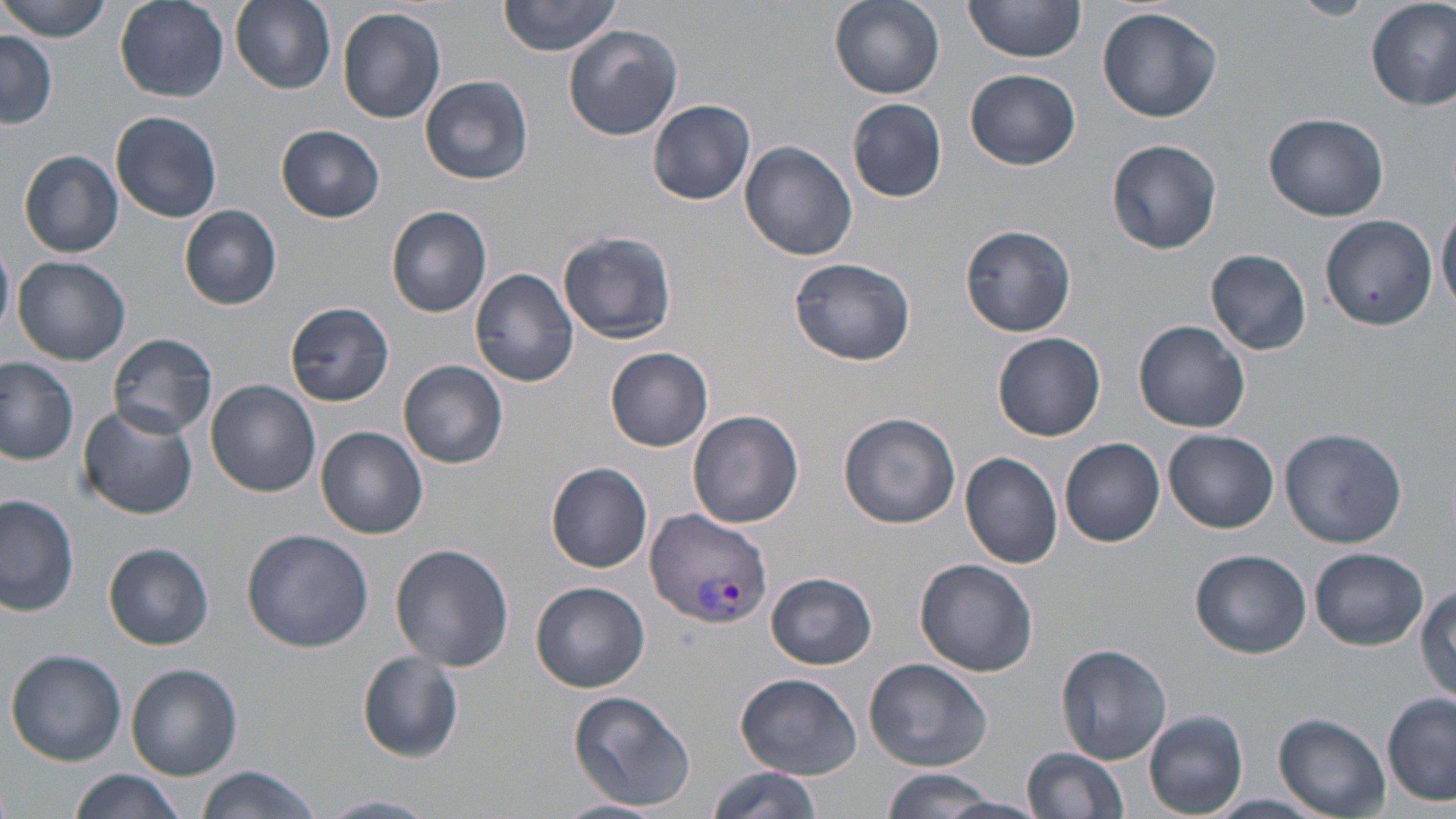 Approximate bounding boxes as named x1/y1/x2/y2 corners in pixels. Uninfected red blood cell locations: (x1=1, y1=0, x2=114, y2=41), (x1=115, y1=0, x2=230, y2=102), (x1=230, y1=0, x2=336, y2=92), (x1=497, y1=0, x2=622, y2=57), (x1=829, y1=0, x2=945, y2=99), (x1=1288, y1=0, x2=1378, y2=21), (x1=1366, y1=0, x2=1456, y2=110), (x1=963, y1=1, x2=1089, y2=67), (x1=1096, y1=5, x2=1224, y2=123), (x1=337, y1=6, x2=447, y2=124), (x1=563, y1=26, x2=683, y2=141), (x1=0, y1=29, x2=57, y2=127), (x1=966, y1=69, x2=1082, y2=168), (x1=420, y1=76, x2=533, y2=185), (x1=847, y1=98, x2=948, y2=203), (x1=648, y1=99, x2=756, y2=203), (x1=110, y1=110, x2=224, y2=222), (x1=1263, y1=111, x2=1387, y2=221), (x1=275, y1=125, x2=386, y2=222), (x1=1106, y1=139, x2=1223, y2=255), (x1=740, y1=142, x2=857, y2=260), (x1=19, y1=150, x2=124, y2=257), (x1=1437, y1=199, x2=1456, y2=314), (x1=179, y1=204, x2=282, y2=309), (x1=386, y1=207, x2=492, y2=317), (x1=1319, y1=215, x2=1436, y2=331), (x1=960, y1=223, x2=1077, y2=337), (x1=559, y1=228, x2=677, y2=346), (x1=0, y1=242, x2=14, y2=339), (x1=1206, y1=248, x2=1312, y2=356), (x1=788, y1=254, x2=914, y2=366), (x1=13, y1=256, x2=130, y2=366), (x1=469, y1=268, x2=580, y2=389), (x1=285, y1=302, x2=395, y2=406), (x1=1135, y1=319, x2=1251, y2=432), (x1=109, y1=331, x2=218, y2=439), (x1=994, y1=331, x2=1106, y2=440), (x1=606, y1=347, x2=714, y2=451), (x1=0, y1=358, x2=78, y2=465), (x1=399, y1=361, x2=508, y2=468), (x1=205, y1=378, x2=320, y2=496), (x1=78, y1=404, x2=198, y2=519), (x1=689, y1=410, x2=805, y2=528), (x1=839, y1=412, x2=960, y2=528), (x1=317, y1=426, x2=427, y2=540), (x1=1279, y1=426, x2=1407, y2=547), (x1=1164, y1=431, x2=1278, y2=533), (x1=1060, y1=438, x2=1166, y2=547), (x1=959, y1=450, x2=1064, y2=568), (x1=546, y1=463, x2=653, y2=573), (x1=0, y1=495, x2=79, y2=615), (x1=240, y1=528, x2=373, y2=651), (x1=104, y1=543, x2=213, y2=649), (x1=390, y1=543, x2=513, y2=672), (x1=1309, y1=546, x2=1430, y2=649), (x1=1190, y1=549, x2=1309, y2=656), (x1=914, y1=558, x2=1038, y2=677), (x1=768, y1=572, x2=878, y2=669), (x1=530, y1=581, x2=650, y2=692), (x1=1414, y1=581, x2=1456, y2=700), (x1=1057, y1=643, x2=1172, y2=764), (x1=6, y1=649, x2=127, y2=765), (x1=357, y1=651, x2=464, y2=762), (x1=864, y1=657, x2=991, y2=770), (x1=126, y1=664, x2=242, y2=779), (x1=735, y1=672, x2=862, y2=779), (x1=567, y1=690, x2=696, y2=811), (x1=1382, y1=692, x2=1455, y2=805), (x1=1143, y1=710, x2=1247, y2=816), (x1=1273, y1=712, x2=1391, y2=815), (x1=1021, y1=746, x2=1131, y2=819), (x1=195, y1=766, x2=326, y2=819), (x1=708, y1=766, x2=823, y2=819), (x1=69, y1=769, x2=185, y2=819), (x1=879, y1=769, x2=1010, y2=817), (x1=318, y1=794, x2=439, y2=818), (x1=1206, y1=794, x2=1327, y2=817), (x1=935, y1=795, x2=1051, y2=819), (x1=555, y1=799, x2=664, y2=819). Plasmodium vivax-infected red blood cell locations: (x1=643, y1=509, x2=772, y2=629). Slide-level diagnosis: Plasmodium vivax. Image is 1456×819 pixels. Single field of view. Captured at 1000x magnification. Light microscopy. May-Grünwald-Giemsa-stained preparation. Thin blood film.